Identify the cell.
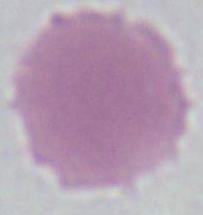
This is an erythrocyte.

{
  "magnification": "1000x",
  "modality": "photomicrograph"
}